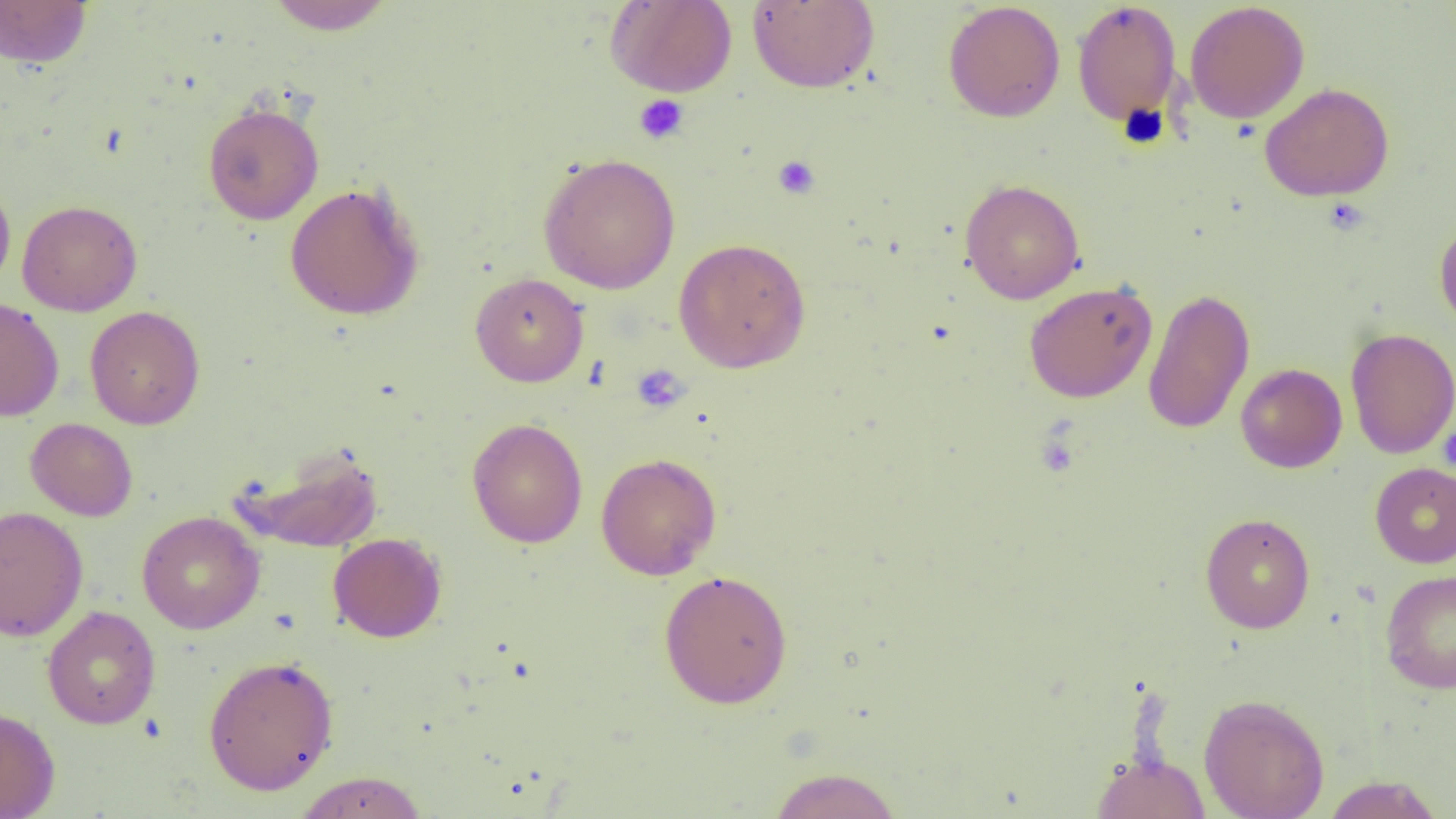 Approximate bounding boxes as named x1/y1/x2/y2 corners in pixels. Uninfected red blood cell locations: (x1=265, y1=0, x2=396, y2=35), (x1=605, y1=0, x2=737, y2=97), (x1=0, y1=1, x2=93, y2=68), (x1=747, y1=1, x2=880, y2=93), (x1=942, y1=1, x2=1066, y2=123), (x1=1072, y1=1, x2=1182, y2=127), (x1=1184, y1=2, x2=1309, y2=124), (x1=1260, y1=82, x2=1394, y2=202), (x1=202, y1=101, x2=324, y2=225), (x1=538, y1=152, x2=681, y2=294), (x1=0, y1=176, x2=16, y2=293), (x1=959, y1=179, x2=1085, y2=304), (x1=284, y1=182, x2=425, y2=321), (x1=16, y1=199, x2=143, y2=316), (x1=1434, y1=218, x2=1456, y2=333), (x1=673, y1=238, x2=811, y2=373), (x1=470, y1=272, x2=589, y2=387), (x1=1024, y1=281, x2=1157, y2=403), (x1=1142, y1=287, x2=1255, y2=434), (x1=0, y1=297, x2=64, y2=422), (x1=85, y1=305, x2=205, y2=430), (x1=1345, y1=327, x2=1456, y2=458), (x1=1235, y1=363, x2=1347, y2=473), (x1=466, y1=417, x2=588, y2=548), (x1=25, y1=418, x2=138, y2=521), (x1=237, y1=445, x2=384, y2=554), (x1=596, y1=452, x2=722, y2=580), (x1=1370, y1=462, x2=1456, y2=568), (x1=0, y1=505, x2=89, y2=642), (x1=137, y1=511, x2=265, y2=634), (x1=1200, y1=512, x2=1315, y2=633), (x1=328, y1=532, x2=446, y2=643), (x1=658, y1=569, x2=793, y2=709), (x1=1380, y1=569, x2=1456, y2=694), (x1=42, y1=605, x2=161, y2=730), (x1=202, y1=654, x2=339, y2=794), (x1=1199, y1=693, x2=1329, y2=818), (x1=0, y1=706, x2=60, y2=818), (x1=1092, y1=752, x2=1210, y2=818), (x1=766, y1=767, x2=903, y2=819), (x1=292, y1=771, x2=430, y2=818), (x1=1321, y1=775, x2=1444, y2=818). Platelet locations: (x1=634, y1=94, x2=689, y2=144), (x1=773, y1=155, x2=820, y2=199), (x1=1324, y1=198, x2=1370, y2=235), (x1=631, y1=364, x2=689, y2=413), (x1=1438, y1=422, x2=1456, y2=473). Slide-level diagnosis: negative for blood parasites. Optical microscopy. Single field of view. Thin blood film. Captured at 1000x magnification. Image is 1456×819 pixels.